Comment on the morphology of the erythrocytes.
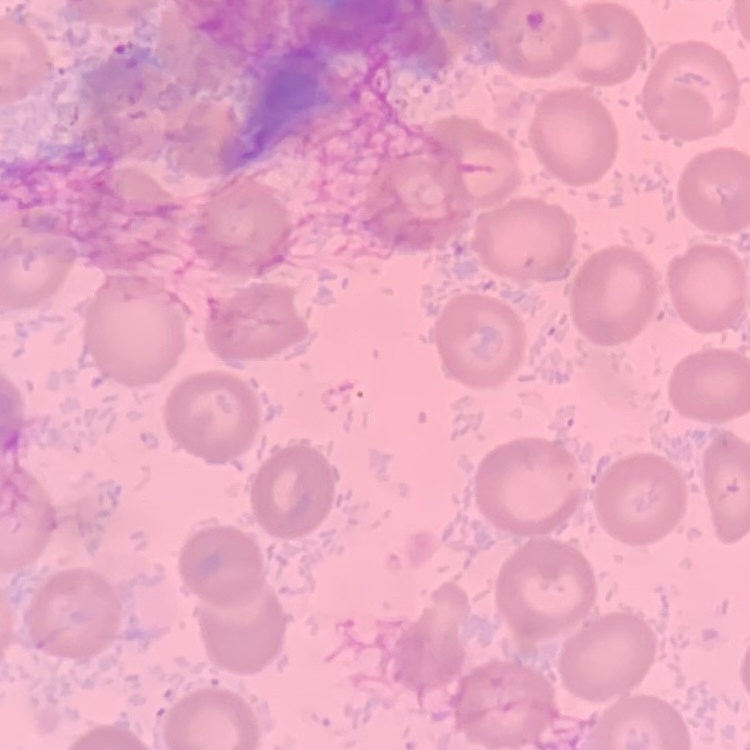

They show no rouleaux formation.

{
  "preparation": "thin peripheral smear",
  "stain": "Field's or Giemsa",
  "image_type": "one tile cut from a larger photomicrograph"
}